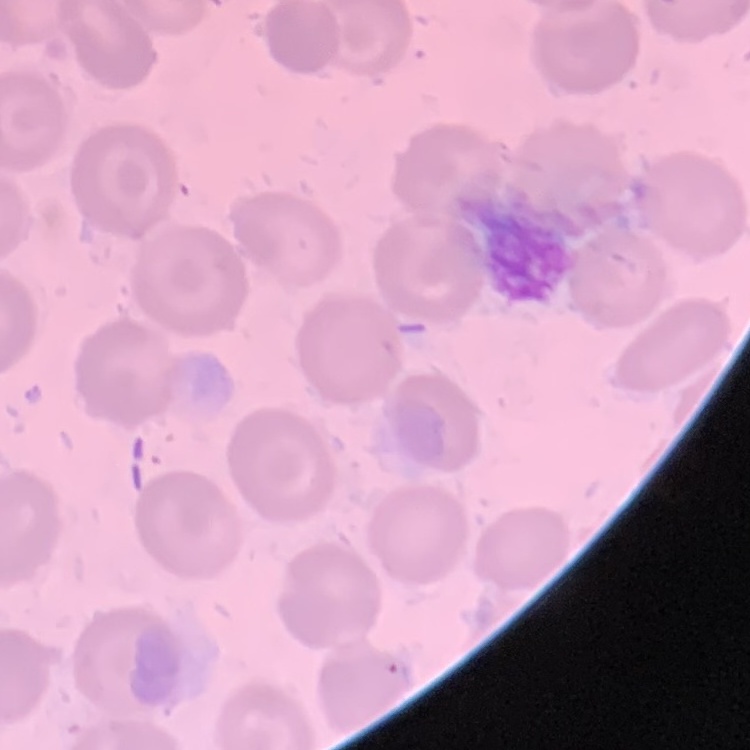
Summary:
  - Erythrocyte morphology: no rouleaux formation
  - Stain: Field's or Giemsa
  - Preparation: thin blood smear
  - Image type: square crop of a larger photomicrograph